Describe the morphology of the red blood cells.
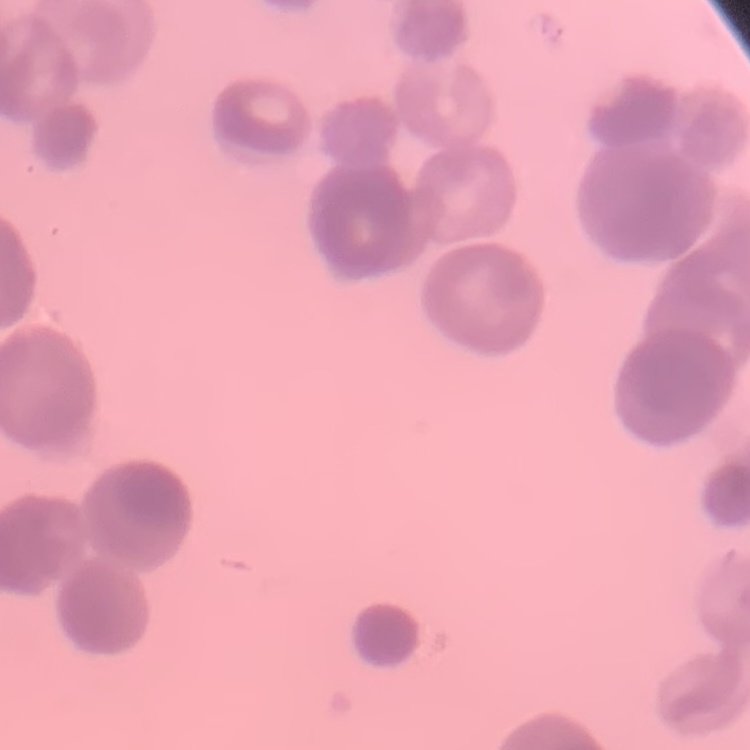
Rouleaux formation.

stain: Field's or Giemsa
preparation: thin blood smear
image_type: square crop of a larger photomicrograph